Point out each Plasmodium parasite.
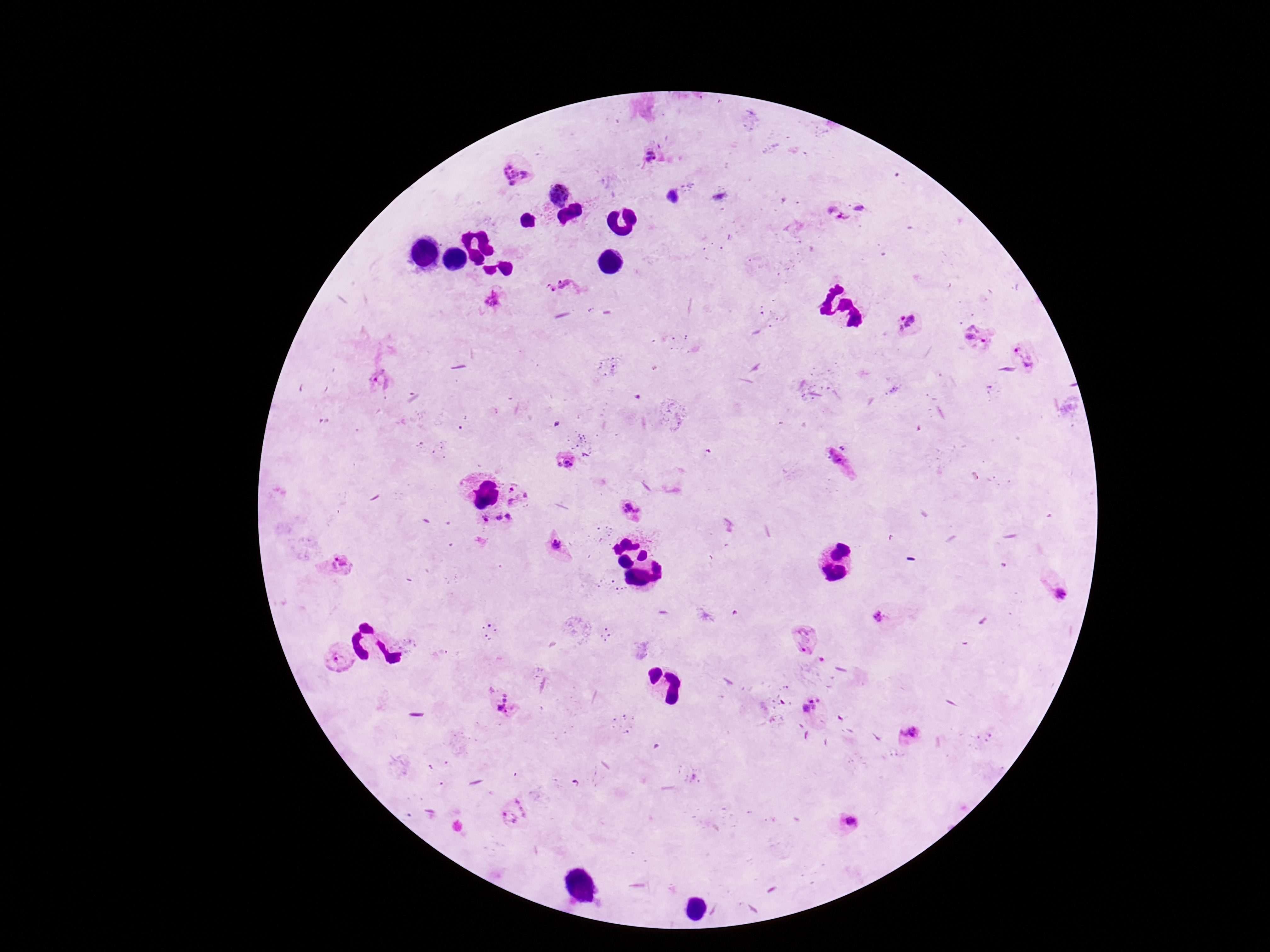

Approximate centers as {x, y} in pixels.
Plasmodium parasites: {653, 153}, {512, 173}, {558, 194}, {672, 196}, {862, 208}, {837, 214}, {564, 287}, {490, 299}, {907, 321}, {978, 337}, {1026, 354}, {381, 381}, {564, 460}, {517, 496}, {635, 506}, {497, 519}, {556, 545}, {337, 570}, {1060, 591}, {878, 617}, {804, 640}, {337, 659}, {501, 705}, {814, 707}, {908, 732}, {513, 811}, {850, 821}.

capture = smartphone camera through the microscope eyepiece
image size = 1270×952 pixels
magnification = 100x
preparation = thick blood film
field of view = single
stain = Giemsa
patient malaria status = infected